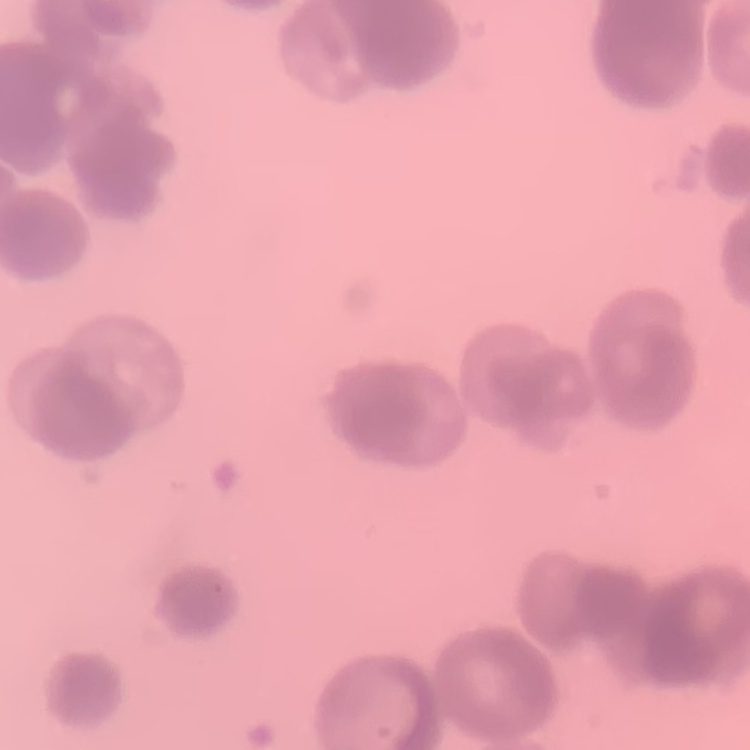

The red blood cells show rouleaux formation. Thin peripheral smear. Field's or Giemsa stain. One tile cut from a larger photomicrograph.